Locate every blood parasite and identify its species.
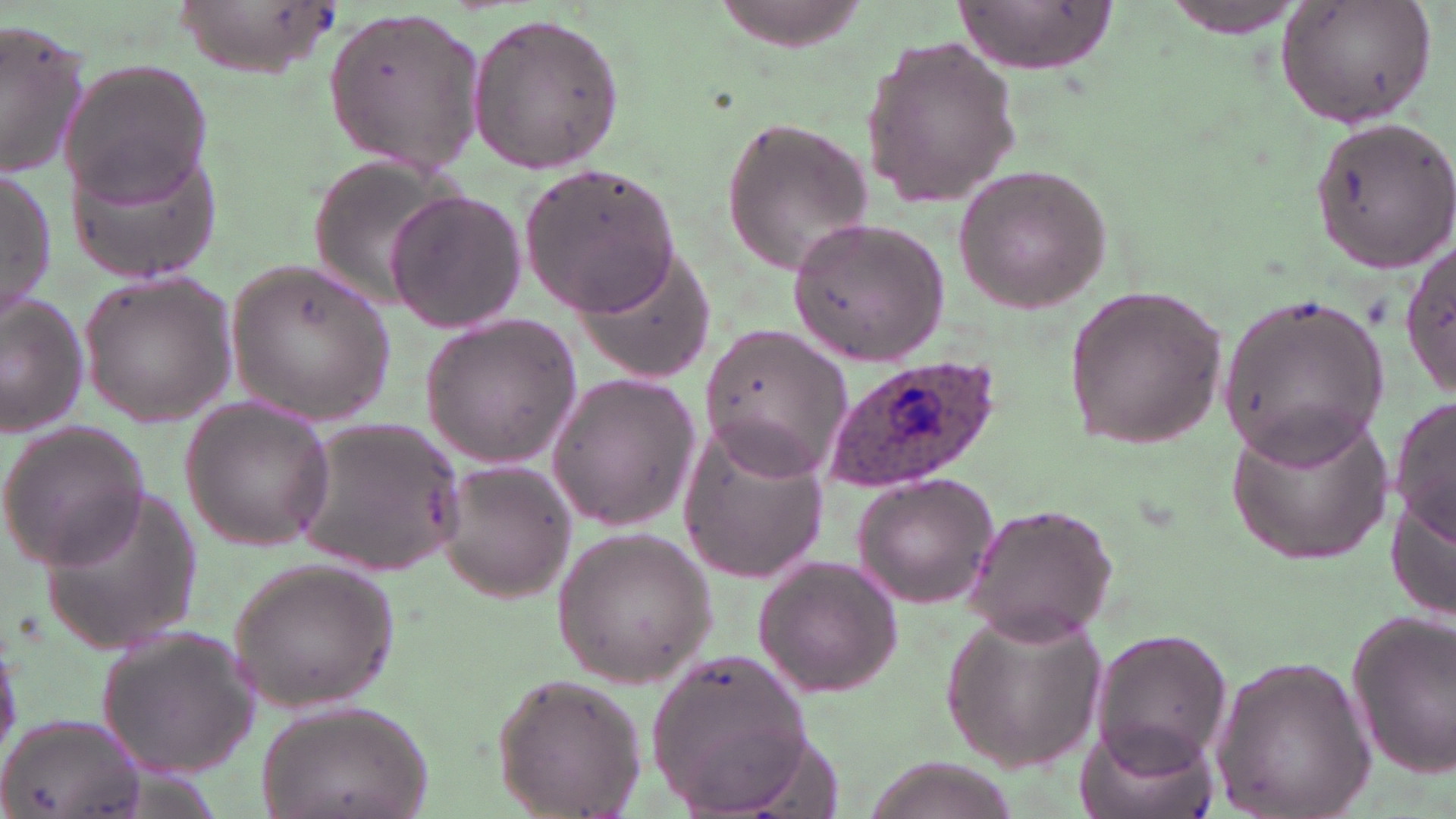

Approximate bounding boxes as named x1/y1/x2/y2 corners in pixels.
Plasmodium ovale-infected red blood cells: (x1=820, y1=354, x2=1003, y2=494).
No Plasmodium falciparum, Plasmodium malariae, Plasmodium vivax, Babesia divergens, or Trypanosoma brucei observed.

Summary:
  - Uninfected red blood cell locations: (x1=166, y1=1, x2=349, y2=75), (x1=952, y1=1, x2=1122, y2=72), (x1=1157, y1=2, x2=1307, y2=37), (x1=1275, y1=2, x2=1438, y2=128), (x1=317, y1=5, x2=490, y2=175), (x1=465, y1=13, x2=628, y2=173), (x1=0, y1=20, x2=91, y2=179), (x1=859, y1=36, x2=1022, y2=210), (x1=61, y1=59, x2=212, y2=210), (x1=717, y1=113, x2=876, y2=277), (x1=1307, y1=117, x2=1456, y2=274), (x1=64, y1=137, x2=226, y2=287), (x1=308, y1=151, x2=476, y2=311), (x1=519, y1=159, x2=685, y2=317), (x1=0, y1=165, x2=55, y2=318), (x1=955, y1=166, x2=1110, y2=310), (x1=387, y1=190, x2=527, y2=335), (x1=787, y1=216, x2=950, y2=368), (x1=1402, y1=237, x2=1452, y2=402), (x1=571, y1=241, x2=719, y2=386), (x1=223, y1=258, x2=395, y2=426), (x1=78, y1=271, x2=236, y2=424), (x1=1062, y1=285, x2=1227, y2=451), (x1=1217, y1=294, x2=1395, y2=462), (x1=1, y1=295, x2=91, y2=435), (x1=418, y1=315, x2=581, y2=468), (x1=700, y1=323, x2=852, y2=481), (x1=544, y1=371, x2=702, y2=531), (x1=1391, y1=394, x2=1454, y2=550), (x1=179, y1=399, x2=334, y2=552), (x1=1225, y1=408, x2=1394, y2=567), (x1=289, y1=417, x2=470, y2=575), (x1=0, y1=420, x2=153, y2=572), (x1=679, y1=425, x2=831, y2=582), (x1=439, y1=458, x2=576, y2=605), (x1=852, y1=472, x2=1000, y2=611), (x1=31, y1=480, x2=204, y2=652), (x1=957, y1=501, x2=1122, y2=645), (x1=552, y1=525, x2=718, y2=690), (x1=751, y1=553, x2=903, y2=698), (x1=226, y1=556, x2=398, y2=713), (x1=938, y1=606, x2=1110, y2=772), (x1=1345, y1=609, x2=1456, y2=779), (x1=97, y1=625, x2=264, y2=777), (x1=1090, y1=628, x2=1231, y2=769), (x1=650, y1=650, x2=813, y2=811), (x1=1207, y1=653, x2=1375, y2=819), (x1=489, y1=674, x2=647, y2=818), (x1=253, y1=699, x2=437, y2=819), (x1=1, y1=711, x2=147, y2=819), (x1=1076, y1=714, x2=1218, y2=819), (x1=868, y1=756, x2=1005, y2=819)
  - Slide-level diagnosis: Plasmodium ovale
  - Field of view: one of a larger specimen
  - Image size: 1456×819 pixels
  - Modality: optical microscopy
  - Preparation: thin blood film
  - Stain: May-Grünwald-Giemsa
  - Magnification: 1000x